Report the malaria status of this cell.
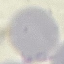

Uninfected.

Summary:
  - Preparation: thin blood film
  - Stain: Giemsa
  - Capture: smartphone camera at the microscope eyepiece
  - Image type: cell patch, automatically extracted from a larger field of view and resized to 64 × 64 pixels